Name the parasite shown.
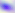

This is Toxoplasma gondii.

Photomicrograph. Captured at 400x magnification.